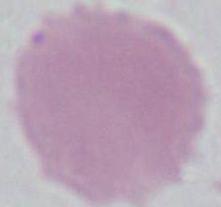
{
  "identification": "red blood cell",
  "magnification": "1000x",
  "modality": "micrograph"
}